Classify this cell by malaria status.
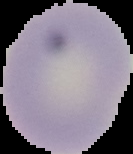

It is uninfected.

preparation = thin blood film
image size = 133×154 pixels
image type = segmented cell region with the area outside set to black